Outline each blood parasite and name the species.
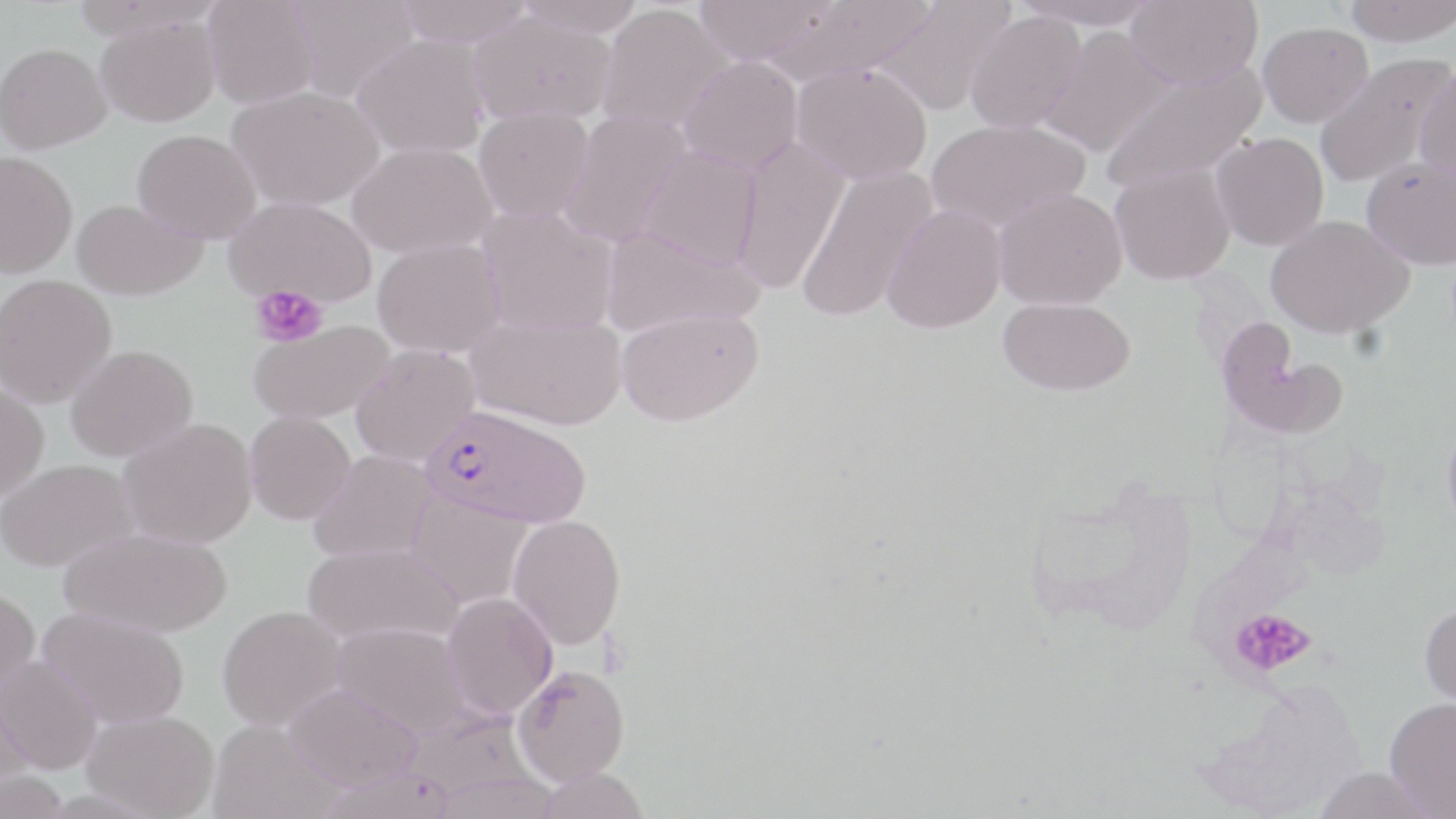

Approximate bounding boxes as (x1, y1, x2, y2) in pixels.
Plasmodium falciparum-infected red blood cells: (421, 403, 592, 528).
No Plasmodium ovale, Plasmodium malariae, Plasmodium vivax, Babesia divergens, or Trypanosoma brucei observed.

slide-level diagnosis = Plasmodium falciparum
modality = light microscopy
uninfected red blood cell locations = approximate bounding boxes as (x1, y1, x2, y2) in pixels: (286, 0, 418, 103), (395, 0, 533, 48), (514, 0, 644, 37), (693, 0, 839, 66), (766, 0, 936, 86), (874, 0, 1015, 115), (1011, 0, 1162, 30), (1125, 0, 1263, 89), (1343, 0, 1456, 46), (203, 1, 320, 109), (597, 5, 731, 134), (468, 11, 616, 126), (964, 11, 1087, 133), (94, 13, 221, 127), (1257, 21, 1373, 127), (1038, 26, 1174, 157), (352, 35, 490, 158), (0, 42, 111, 154), (1313, 51, 1454, 188), (678, 56, 803, 174), (1101, 59, 1267, 192), (792, 61, 932, 184), (1414, 62, 1456, 182), (228, 87, 383, 211), (474, 105, 594, 224), (559, 110, 692, 247), (924, 118, 1090, 233), (132, 129, 261, 243), (1210, 132, 1329, 251), (731, 136, 849, 295), (348, 141, 497, 259), (638, 145, 762, 269), (0, 151, 78, 277), (1361, 155, 1456, 269), (1110, 163, 1235, 285), (796, 165, 938, 324), (993, 187, 1127, 310), (223, 196, 377, 307), (71, 199, 206, 301), (881, 204, 1007, 333), (477, 205, 618, 336), (1265, 214, 1414, 338), (601, 224, 762, 336), (372, 238, 505, 357), (0, 274, 117, 407), (998, 297, 1135, 395), (616, 307, 763, 426), (465, 311, 626, 430), (249, 319, 393, 423), (1216, 322, 1348, 440), (350, 344, 479, 466), (65, 345, 198, 462), (0, 382, 49, 500), (244, 411, 356, 525), (1442, 414, 1456, 537), (118, 418, 257, 548), (309, 450, 438, 562), (0, 458, 138, 572), (1020, 472, 1200, 636), (406, 492, 532, 608), (508, 514, 626, 650), (59, 527, 232, 638), (303, 540, 464, 646), (0, 585, 40, 701), (442, 591, 558, 718), (1419, 601, 1456, 718), (217, 605, 348, 731), (38, 607, 190, 729), (332, 621, 470, 738), (0, 655, 103, 775), (511, 664, 630, 785), (1193, 675, 1372, 819), (0, 683, 36, 795), (283, 683, 422, 792), (1383, 697, 1456, 817), (82, 710, 220, 818), (208, 719, 340, 818), (1312, 765, 1442, 819), (533, 767, 650, 819)
preparation = thin blood smear
field of view = single
magnification = 1000x
image size = 1456×819 pixels
stain = May-Grünwald-Giemsa
platelet locations = approximate bounding boxes as (x1, y1, x2, y2) in pixels: (251, 285, 328, 348), (1229, 607, 1316, 678)